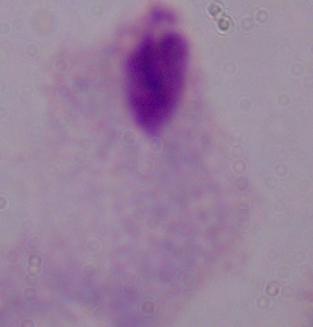

Captured at 1000x magnification. A trichomonad is seen. Micrograph.